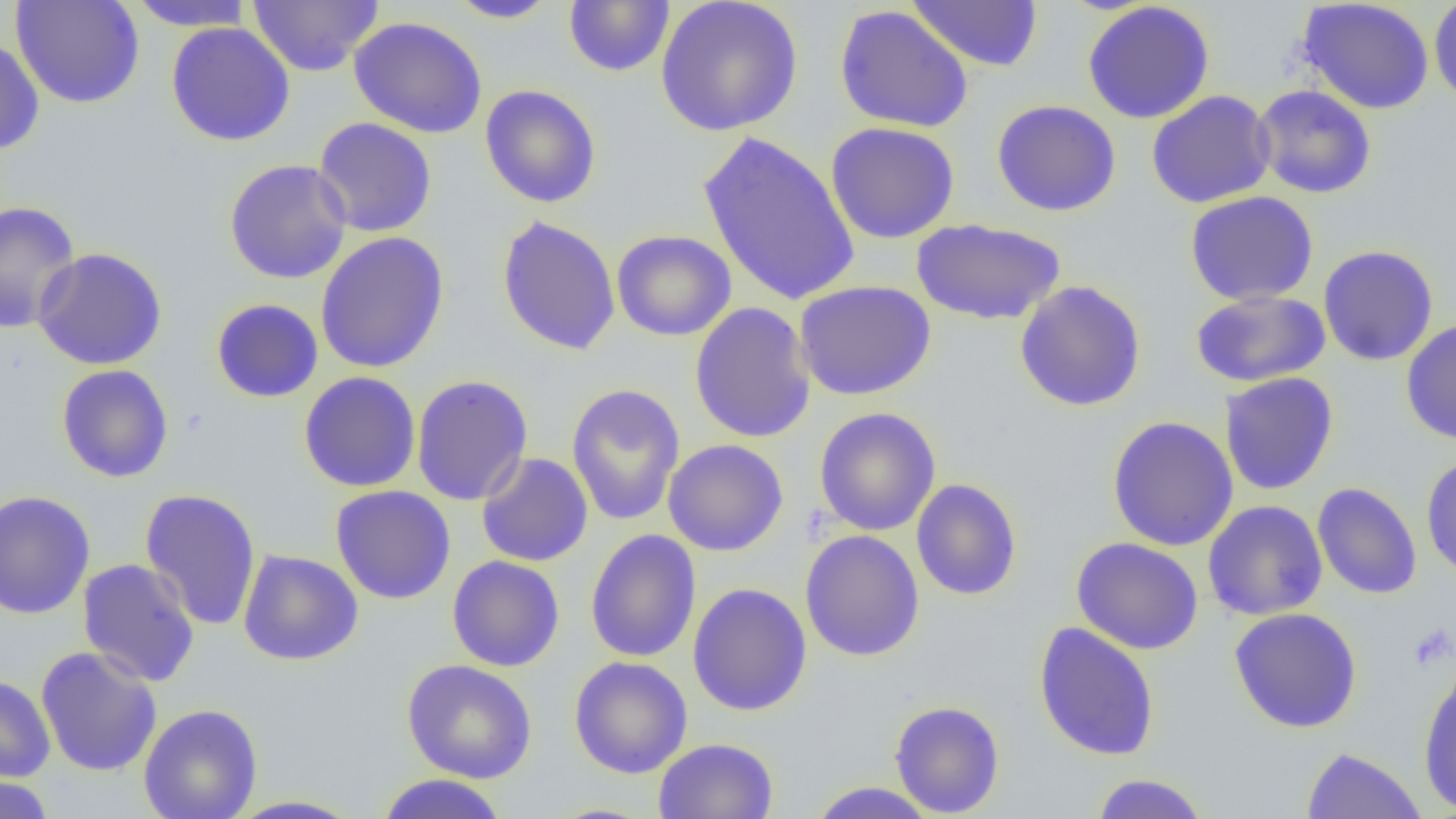
Summary:
  - Coordinate format: approximate bounding boxes as [x1, y1, x2, y2] in pixels
  - Uninfected red blood cell locations: [10, 0, 145, 109], [247, 0, 383, 76], [656, 0, 803, 137], [1297, 0, 1435, 115], [1428, 0, 1456, 109], [126, 1, 255, 30], [444, 1, 560, 23], [563, 1, 675, 76], [907, 1, 1043, 72], [1082, 1, 1216, 124], [834, 5, 974, 133], [348, 16, 487, 139], [166, 21, 296, 146], [0, 35, 45, 155], [479, 84, 601, 208], [1251, 84, 1377, 199], [1146, 90, 1276, 209], [991, 99, 1121, 217], [312, 117, 437, 238], [826, 122, 960, 244], [698, 131, 860, 307], [224, 159, 353, 284], [1185, 191, 1319, 306], [0, 201, 81, 334], [496, 215, 621, 356], [910, 218, 1067, 325], [611, 230, 736, 341], [314, 231, 450, 374], [1318, 245, 1439, 366], [31, 248, 168, 370], [794, 280, 936, 401], [1014, 280, 1147, 412], [1190, 289, 1331, 388], [211, 298, 324, 403], [689, 302, 816, 444], [1400, 318, 1456, 445], [56, 364, 174, 483], [298, 372, 421, 492], [1220, 372, 1339, 496], [410, 375, 533, 506], [566, 383, 685, 526], [814, 407, 941, 536], [1106, 416, 1239, 552], [663, 439, 788, 556], [476, 452, 593, 567], [1420, 454, 1456, 581], [911, 478, 1022, 601], [1312, 482, 1422, 599], [330, 485, 457, 605], [140, 488, 262, 631], [0, 489, 96, 619], [1203, 500, 1328, 621], [585, 530, 702, 663], [800, 530, 925, 662], [1071, 537, 1204, 655], [237, 548, 363, 666], [447, 555, 565, 672], [77, 558, 200, 687], [687, 582, 812, 716], [1229, 607, 1363, 732], [1033, 622, 1160, 761], [35, 646, 162, 777], [568, 656, 693, 779], [402, 659, 538, 783], [1418, 661, 1456, 815], [0, 674, 56, 782], [889, 700, 1005, 817], [139, 703, 263, 819], [653, 737, 779, 819], [1301, 746, 1427, 818], [374, 773, 509, 818], [1089, 773, 1211, 818], [0, 775, 55, 819], [806, 782, 939, 818], [223, 794, 368, 818]
  - Platelet locations: [1408, 623, 1455, 672]
  - Slide-level diagnosis: negative for blood parasites
  - Preparation: thin blood smear
  - Modality: light microscopy
  - Image size: 1456×819 pixels
  - Field of view: single
  - Magnification: 1000x